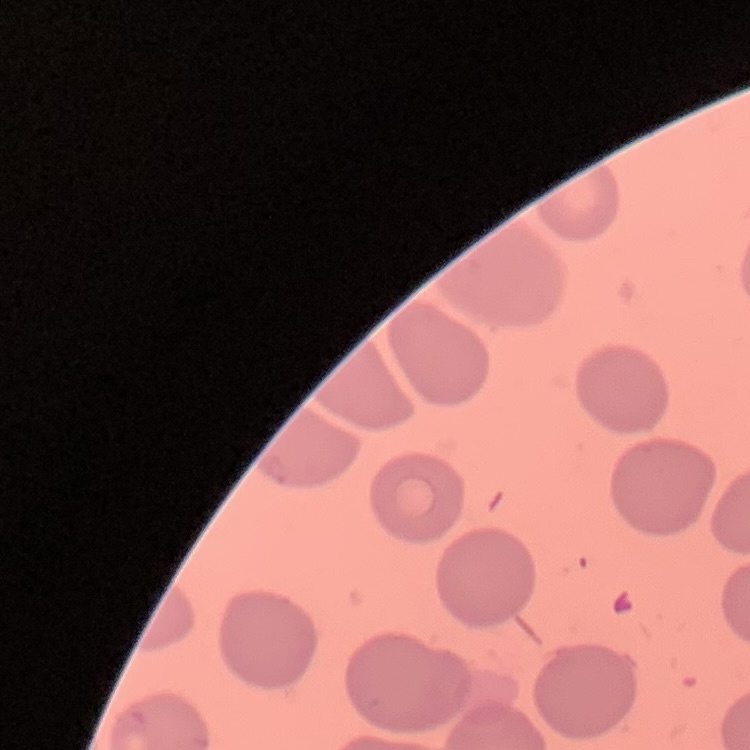

erythrocyte morphology = no rouleaux formation
preparation = thin blood film
image type = one tile cut from a larger photomicrograph
stain = Field's or Giemsa